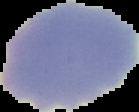 From a thin blood smear. The area outside the segmented cell region is set to black. Image is 139×112 pixels. Result: no malaria parasites detected.